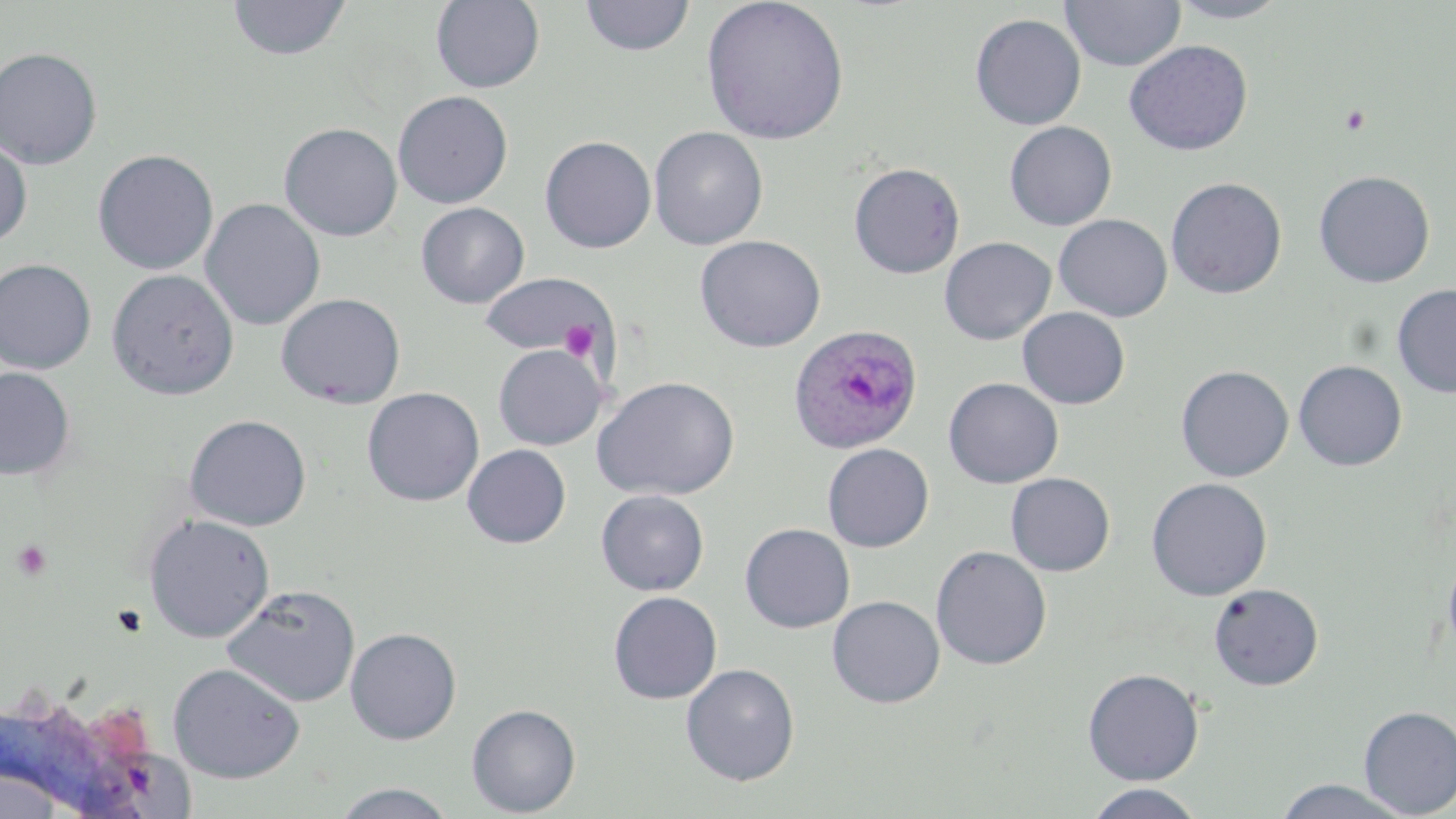

Approximate bounding boxes as (x1,y1)-(x2,y2) corner pairs in pixels. Platelet locations: (1339,105)-(1371,135), (559,319)-(599,361), (11,539)-(53,582), (111,605)-(148,638). Uninfected red blood cell locations: (580,0)-(695,57), (701,0)-(850,146), (1059,0)-(1186,72), (1166,0)-(1292,23), (228,1)-(351,61), (431,1)-(545,93), (970,13)-(1086,130), (1124,40)-(1253,156), (0,47)-(103,170), (392,90)-(513,209), (1004,121)-(1117,231), (279,123)-(402,241), (648,126)-(768,251), (539,135)-(657,253), (0,137)-(32,247), (93,149)-(219,275), (848,162)-(965,279), (1314,170)-(1435,288), (1165,177)-(1287,299), (201,198)-(325,331), (415,202)-(529,309), (1053,214)-(1173,322), (694,235)-(826,353), (939,237)-(1056,345), (0,259)-(96,374), (107,269)-(239,400), (479,273)-(612,356), (1392,284)-(1456,398), (276,293)-(406,409), (1017,307)-(1130,410), (493,344)-(606,450), (1293,360)-(1408,471), (1175,365)-(1294,482), (0,367)-(75,480), (593,376)-(740,501), (942,377)-(1064,489), (362,387)-(484,506), (184,414)-(312,531), (822,443)-(935,552), (462,444)-(571,548), (1005,472)-(1115,576), (1146,478)-(1272,600), (595,489)-(709,596), (143,513)-(276,642), (740,523)-(855,633), (1442,543)-(1456,670), (931,545)-(1052,671), (1208,583)-(1324,691), (221,584)-(361,707), (608,591)-(722,704), (827,595)-(945,708), (345,627)-(462,745), (167,662)-(305,783), (681,663)-(800,785), (1082,667)-(1204,785), (466,703)-(581,817), (1358,705)-(1456,816), (1271,779)-(1413,817), (330,782)-(459,818), (1082,783)-(1206,819). Plasmodium ovale-infected red blood cell locations: (787,323)-(922,454). Slide-level diagnosis: Plasmodium ovale. Thin blood smear. One field of a larger specimen. Light microscopy. Captured at 1000x magnification. Image is 1456×819 pixels. May-Grünwald-Giemsa-stained preparation.